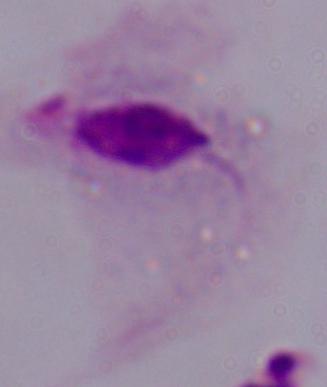
Summary:
  - Magnification: 1000x
  - Modality: photomicrograph
  - Identification: trichomonad